Report the malaria status of this cell.
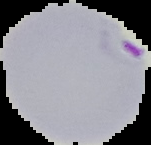
It is parasitized.

Image is 151×145 pixels. The area outside the segmented cell region is set to black. From a thin blood smear.